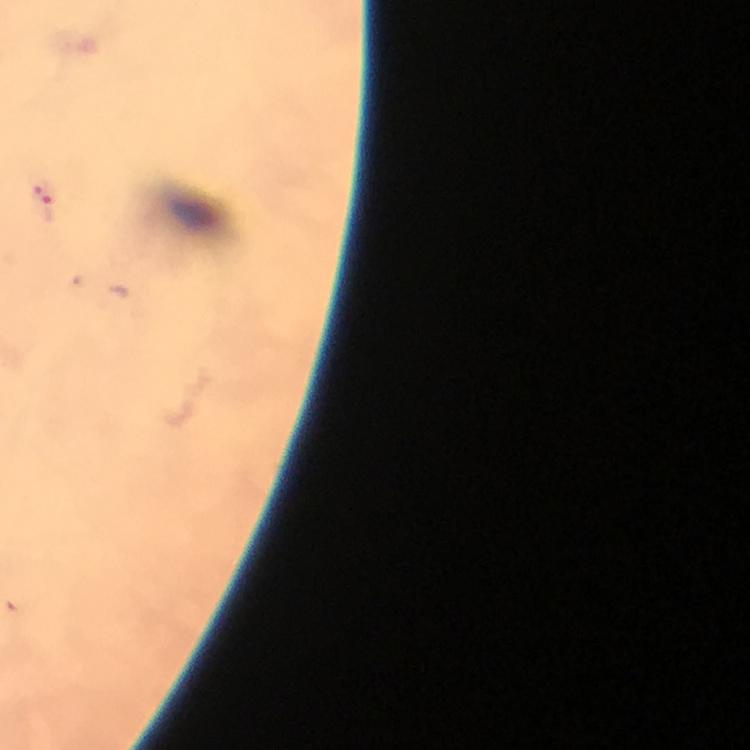

Approximate object centers, in pixels from the top-left corner. Plasmodium parasite locations: (x=47, y=204). Photographed with a smartphone mounted on the microscope. 100x magnification. Image is 750×750 pixels. Thick blood film. A crop from one field of view. Giemsa-stained preparation. Immersion oil was used. From a malaria diagnostic workup.